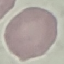
Summary:
  - Malaria status: uninfected
  - Preparation: thin blood smear
  - Capture: smartphone through the microscope eyepiece
  - Image type: cell patch, automatically extracted from a larger field of view and resized to 64 × 64 pixels
  - Stain: Giemsa